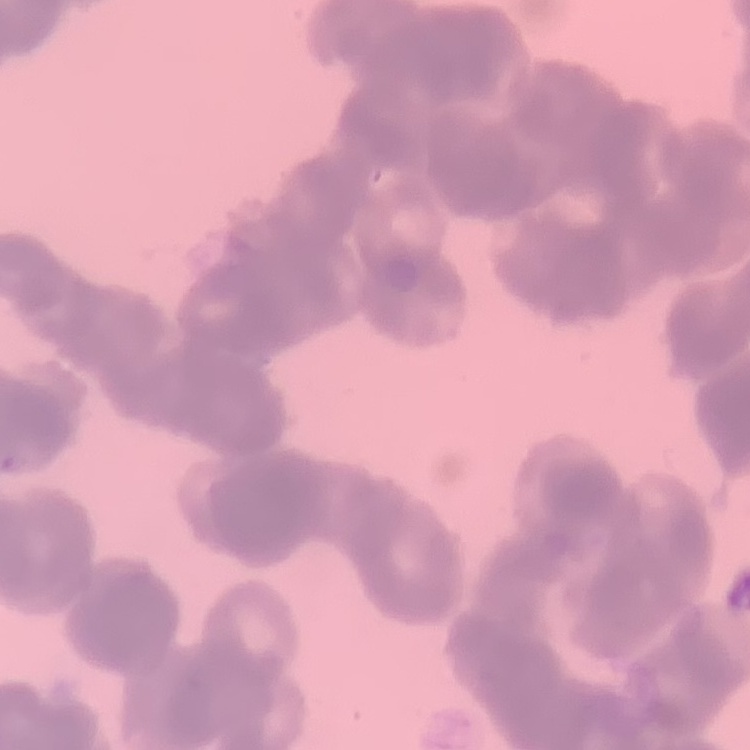
Summary:
  - Red blood cell morphology: rouleaux formation
  - Stain: Field's or Giemsa
  - Preparation: thin blood smear
  - Image type: one tile cut from a larger photomicrograph